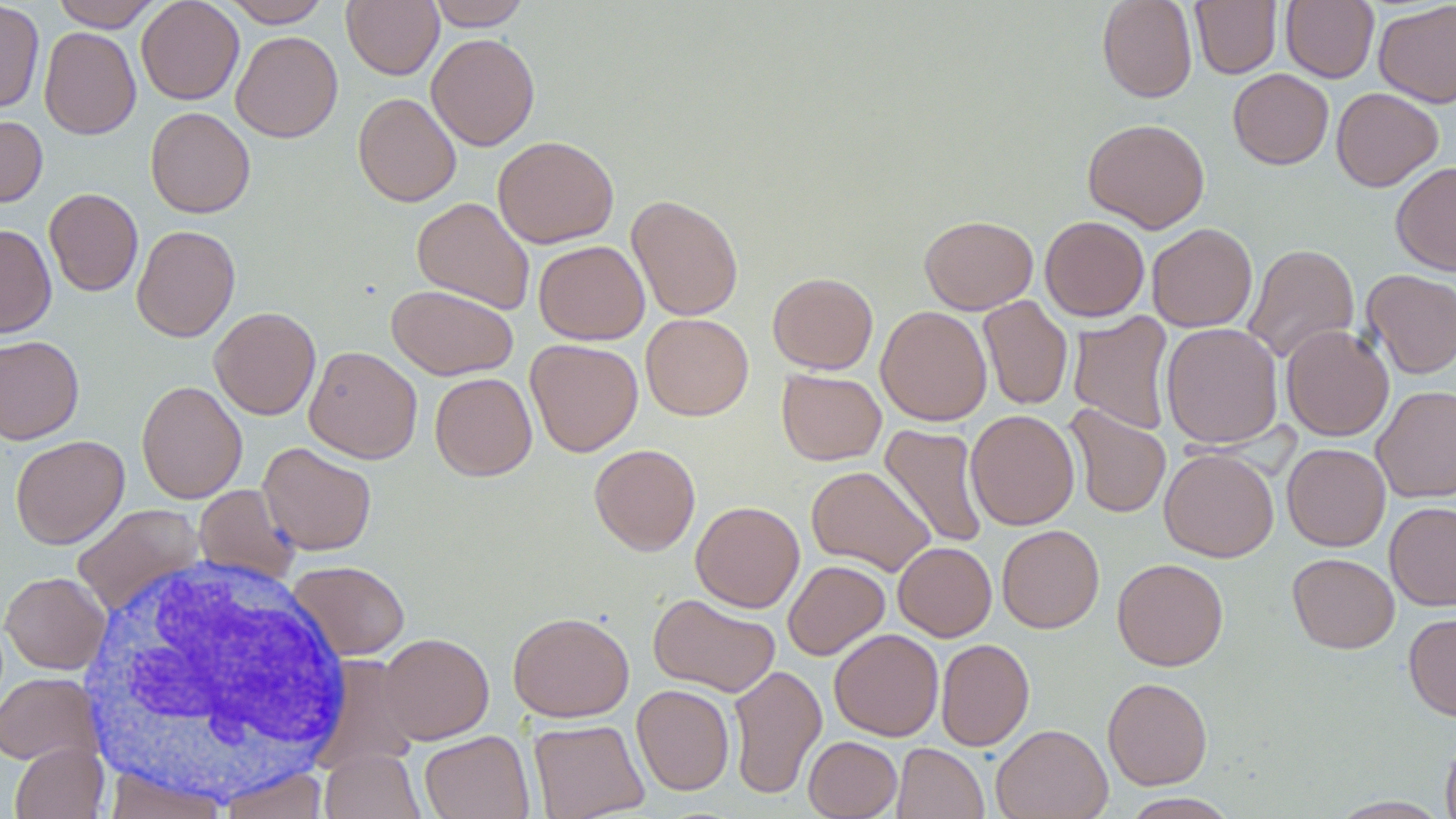
Summary:
  - Coordinate format: approximate bounding boxes as (x1, y1, x2, y2) in pixels
  - Uninfected red blood cell locations: (51, 0, 163, 31), (136, 0, 244, 105), (222, 0, 332, 27), (342, 0, 443, 79), (426, 0, 531, 30), (1097, 0, 1197, 102), (1190, 0, 1281, 78), (1281, 0, 1379, 83), (1373, 0, 1456, 108), (0, 1, 45, 114), (39, 26, 141, 140), (231, 30, 343, 143), (426, 33, 540, 151), (1228, 68, 1334, 170), (1331, 87, 1443, 192), (353, 92, 461, 207), (145, 107, 255, 218), (0, 114, 47, 208), (1082, 118, 1210, 233), (492, 135, 619, 248), (1391, 161, 1456, 275), (44, 188, 143, 296), (626, 194, 744, 321), (412, 197, 535, 315), (919, 214, 1038, 314), (1040, 216, 1150, 321), (1146, 223, 1257, 332), (0, 224, 56, 338), (131, 225, 240, 342), (534, 240, 649, 344), (1243, 243, 1360, 365), (1362, 269, 1456, 378), (767, 272, 878, 374), (387, 284, 518, 380), (978, 296, 1072, 410), (876, 305, 992, 426), (208, 306, 321, 420), (1068, 311, 1175, 435), (640, 313, 754, 420), (1160, 322, 1283, 449), (1281, 325, 1394, 441), (0, 335, 84, 444), (525, 338, 643, 457), (303, 345, 422, 463), (777, 369, 886, 465), (430, 372, 537, 481), (136, 379, 248, 504), (1371, 385, 1456, 503), (1065, 404, 1171, 519), (965, 409, 1080, 530), (879, 424, 989, 549), (10, 434, 129, 549), (258, 442, 377, 555), (589, 443, 701, 556), (1282, 443, 1391, 551), (1159, 448, 1279, 562), (806, 466, 936, 576), (194, 484, 301, 586), (690, 500, 805, 612), (1385, 501, 1456, 610), (72, 503, 205, 616), (997, 525, 1104, 633), (893, 541, 997, 641), (1287, 552, 1400, 653), (1112, 557, 1228, 671), (783, 559, 890, 660), (287, 560, 410, 660), (1, 571, 111, 674), (648, 593, 780, 698), (507, 611, 634, 722), (1404, 611, 1456, 721), (829, 629, 943, 741), (378, 632, 494, 744), (935, 638, 1034, 751), (728, 664, 827, 800), (0, 672, 101, 766), (1102, 677, 1213, 790), (632, 684, 734, 795), (528, 719, 649, 819), (991, 724, 1113, 819), (419, 730, 535, 819), (1440, 735, 1456, 819), (804, 736, 902, 819), (10, 741, 108, 819), (892, 743, 988, 819), (320, 748, 426, 819), (217, 766, 330, 819), (104, 768, 229, 819), (1121, 792, 1240, 818), (1327, 796, 1452, 818)
  - White blood cell locations: (70, 551, 358, 804)
  - Slide-level diagnosis: negative for blood parasites
  - Preparation: thin blood smear
  - Modality: light microscopy
  - Stain: May-Grünwald-Giemsa
  - Field of view: single
  - Magnification: 1000x
  - Image size: 1456×819 pixels